Identify the cell.
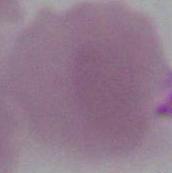
An erythrocyte.

Captured at 1000x magnification. Micrograph.